Report the malaria status of this cell.
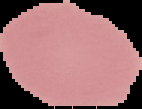
It is uninfected.

The area outside the segmented cell region is set to black. Image is 142×109 pixels. From a thin blood film.